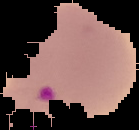
{
  "image_size": "139×130 pixels",
  "result": "Plasmodium parasites detected",
  "image_type": "segmented cell region on a black background",
  "preparation": "thin blood smear"
}